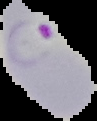
image_type: cell region segmented out of the field of view; surrounding area masked to black
image_size: 97×121 pixels
result: Plasmodium parasites identified
preparation: thin blood smear